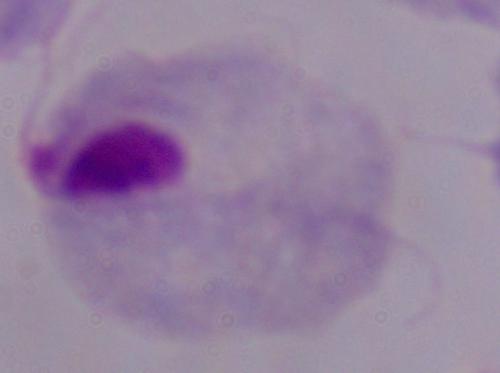
Summary:
  - Magnification: 1000x
  - Modality: photomicrograph
  - Identification: trichomonad